Name the cell type shown.
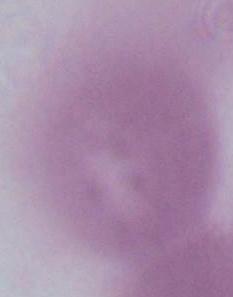
An erythrocyte.

Photomicrograph. 1000x magnification.